Locate every Plasmodium vivax-infected red blood cell.
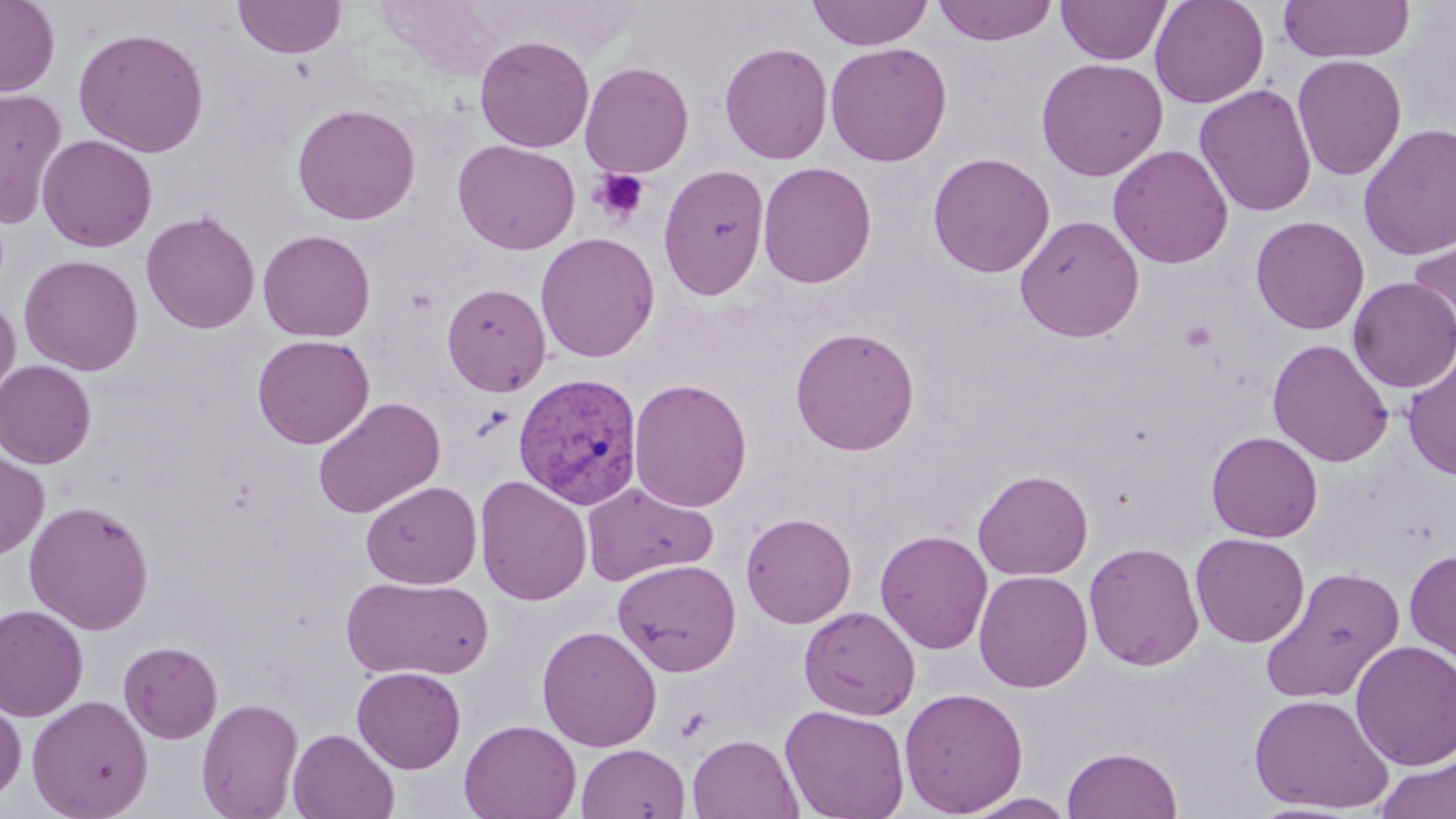

Approximate bounding boxes as named x1/y1/x2/y2 corners in pixels.
Plasmodium vivax-infected red blood cells: (x1=512, y1=372, x2=644, y2=509).

slide-level diagnosis = Plasmodium vivax
modality = light microscopy
field of view = single
image size = 1456×819 pixels
uninfected red blood cell locations = approximate bounding boxes as named x1/y1/x2/y2 corners in pixels: (x1=0, y1=0, x2=60, y2=96), (x1=233, y1=0, x2=347, y2=59), (x1=807, y1=0, x2=933, y2=50), (x1=932, y1=0, x2=1059, y2=46), (x1=1149, y1=0, x2=1270, y2=108), (x1=1277, y1=0, x2=1415, y2=63), (x1=1056, y1=1, x2=1171, y2=64), (x1=73, y1=26, x2=210, y2=157), (x1=474, y1=35, x2=594, y2=152), (x1=719, y1=41, x2=833, y2=165), (x1=825, y1=42, x2=952, y2=167), (x1=1292, y1=54, x2=1407, y2=180), (x1=1035, y1=57, x2=1168, y2=181), (x1=579, y1=60, x2=694, y2=177), (x1=1194, y1=84, x2=1317, y2=218), (x1=0, y1=86, x2=67, y2=228), (x1=291, y1=102, x2=421, y2=225), (x1=1358, y1=123, x2=1456, y2=261), (x1=37, y1=134, x2=158, y2=252), (x1=452, y1=139, x2=581, y2=255), (x1=1108, y1=145, x2=1234, y2=268), (x1=927, y1=152, x2=1055, y2=277), (x1=757, y1=161, x2=877, y2=289), (x1=658, y1=163, x2=770, y2=300), (x1=140, y1=209, x2=260, y2=334), (x1=1015, y1=214, x2=1145, y2=342), (x1=1251, y1=215, x2=1370, y2=335), (x1=257, y1=229, x2=376, y2=342), (x1=1405, y1=231, x2=1456, y2=353), (x1=535, y1=232, x2=659, y2=362), (x1=19, y1=254, x2=144, y2=375), (x1=1349, y1=277, x2=1456, y2=393), (x1=441, y1=282, x2=551, y2=397), (x1=0, y1=295, x2=20, y2=400), (x1=790, y1=326, x2=920, y2=456), (x1=252, y1=334, x2=375, y2=449), (x1=1267, y1=338, x2=1394, y2=467), (x1=1402, y1=349, x2=1456, y2=481), (x1=0, y1=359, x2=97, y2=467), (x1=628, y1=378, x2=753, y2=512), (x1=313, y1=396, x2=446, y2=519), (x1=1206, y1=431, x2=1323, y2=542), (x1=0, y1=451, x2=49, y2=559), (x1=973, y1=469, x2=1093, y2=580), (x1=474, y1=476, x2=592, y2=606), (x1=361, y1=480, x2=482, y2=589), (x1=582, y1=482, x2=719, y2=587), (x1=23, y1=499, x2=154, y2=634), (x1=741, y1=512, x2=857, y2=628), (x1=875, y1=529, x2=993, y2=654), (x1=1190, y1=532, x2=1310, y2=647), (x1=1083, y1=541, x2=1205, y2=671), (x1=1404, y1=549, x2=1456, y2=665), (x1=612, y1=559, x2=741, y2=677), (x1=1260, y1=566, x2=1405, y2=704), (x1=974, y1=570, x2=1093, y2=693), (x1=342, y1=575, x2=493, y2=681), (x1=0, y1=604, x2=88, y2=722), (x1=799, y1=606, x2=921, y2=720), (x1=537, y1=624, x2=662, y2=752), (x1=1351, y1=639, x2=1456, y2=769), (x1=118, y1=641, x2=223, y2=743), (x1=352, y1=666, x2=466, y2=773), (x1=899, y1=687, x2=1029, y2=817), (x1=1248, y1=693, x2=1395, y2=813), (x1=27, y1=695, x2=153, y2=819), (x1=0, y1=696, x2=27, y2=803), (x1=196, y1=697, x2=304, y2=819), (x1=780, y1=704, x2=910, y2=819), (x1=460, y1=719, x2=581, y2=819), (x1=288, y1=728, x2=400, y2=818), (x1=687, y1=734, x2=803, y2=819), (x1=576, y1=743, x2=690, y2=819), (x1=1062, y1=746, x2=1183, y2=819), (x1=1375, y1=755, x2=1456, y2=819), (x1=959, y1=792, x2=1078, y2=818)
preparation = thin blood smear
platelet locations = approximate bounding boxes as named x1/y1/x2/y2 corners in pixels: (x1=588, y1=168, x2=651, y2=225)
magnification = 1000x
stain = May-Grünwald-Giemsa